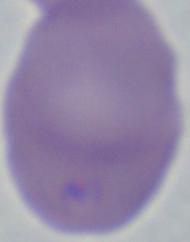
modality: micrograph
identification: Babesia
magnification: 1000x